Give the position of every Plasmodium parasite.
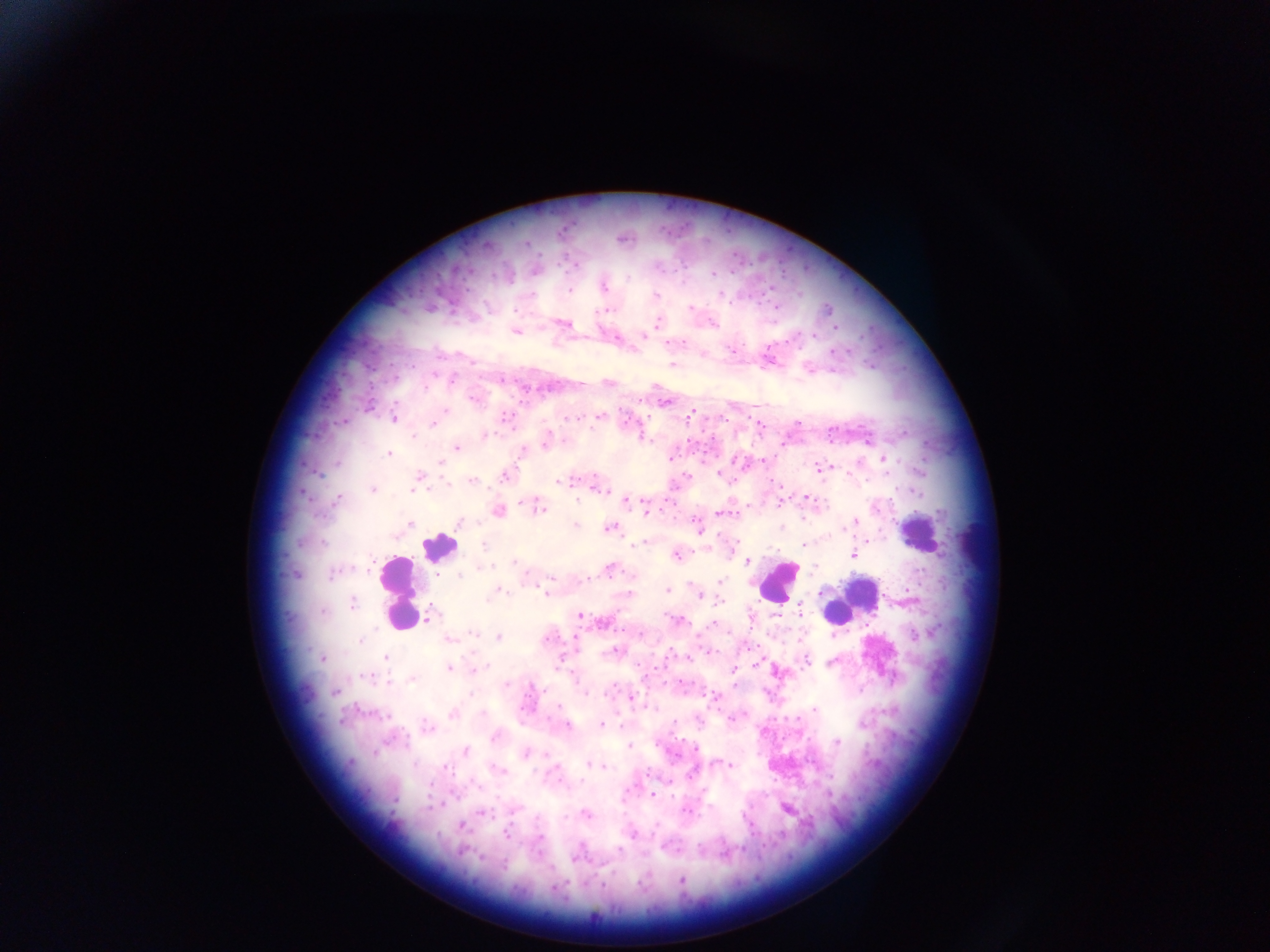
Approximate centers as x y in pixels.
Plasmodium parasites: 622 239; 572 265; 535 271; 603 286; 655 297; 775 305; 691 308; 828 310; 712 323; 564 324; 657 324; 836 328; 516 330; 643 334; 813 335; 616 337; 732 350; 703 355; 768 358; 672 364; 809 368; 608 382; 580 384; 473 399; 664 402; 445 410; 691 412; 600 416; 394 418; 576 418; 433 423; 759 425; 484 435; 867 438; 546 441; 456 446; 522 451; 387 454; 670 458; 884 458; 762 460; 439 461; 821 469; 720 473; 505 474; 417 480; 471 481; 565 481; 597 486; 372 489; 807 497; 336 499; 625 501; 779 504; 537 506; 647 510; 497 511; 724 513; 459 522; 854 522; 410 524; 697 525; 576 526; 609 527; 644 542; 803 544; 853 553; 675 555; 746 561; 610 568; 294 574; 586 579; 719 582; 821 589; 667 590; 495 591; 548 592; 628 593; 699 596; 352 602; 429 616; 579 616; 677 620; 604 621; 714 623; 498 637; 576 637; 449 639; 614 651; 384 657; 687 657; 322 658; 805 661; 756 662; 449 668; 474 669; 734 669; 777 671; 412 678; 735 682; 334 691; 631 698; 813 709; 452 713; 600 725; 566 726; 426 727; 496 737; 837 742; 465 750; 526 754; 724 763; 592 764; 729 764; 653 794; 787 808; 511 809; 482 812; 585 814; 459 825; 632 833; 506 834; 540 838; 577 856; 682 882.

image size = 1270×952 pixels
leukocyte locations = approximate centers as x y in pixels: 919 533; 439 547; 776 582; 401 591; 849 601
preparation = thick blood smear
country = Ghana
capture = mobile-phone photograph through a microscope
field of view = single